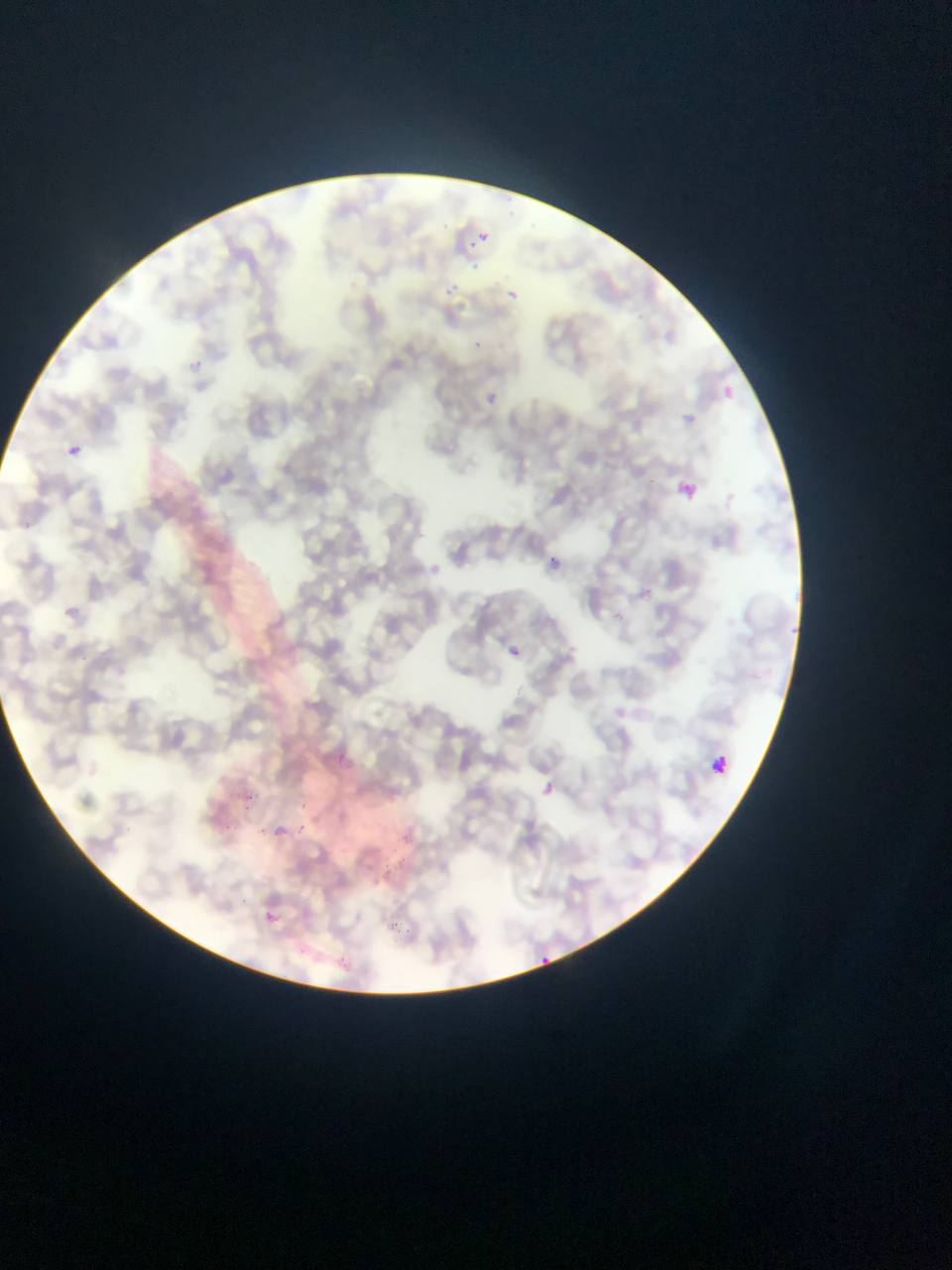

Approximate bounding boxes as left top right bottom in pixels. Malaria parasite locations: 510 207 522 224; 476 215 496 239; 468 241 480 254; 443 282 462 298; 503 288 516 299; 472 341 486 354; 726 381 739 396; 488 390 503 403; 67 444 82 457; 677 478 698 500; 546 555 566 571; 89 575 101 587; 65 606 79 617; 507 640 522 661; 540 777 559 796; 247 795 266 812; 221 812 236 831; 298 815 312 830; 261 909 284 932; 392 919 418 940; 538 949 551 966. Leukocyte locations: 707 754 733 779. Photographed through a microscope with a mobile-phone camera. Collected in Ghana. Thin blood smear. Image is 952×1270 pixels. Single field of view.